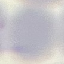 Malaria status: uninfected. Photographed with a smartphone camera at the microscope eyepiece. Automatically extracted cell patch, resized to 64 × 64 pixels. Thin blood smear. Giemsa-stained preparation.